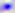
magnification: 400x
modality: micrograph
identification: Toxoplasma gondii